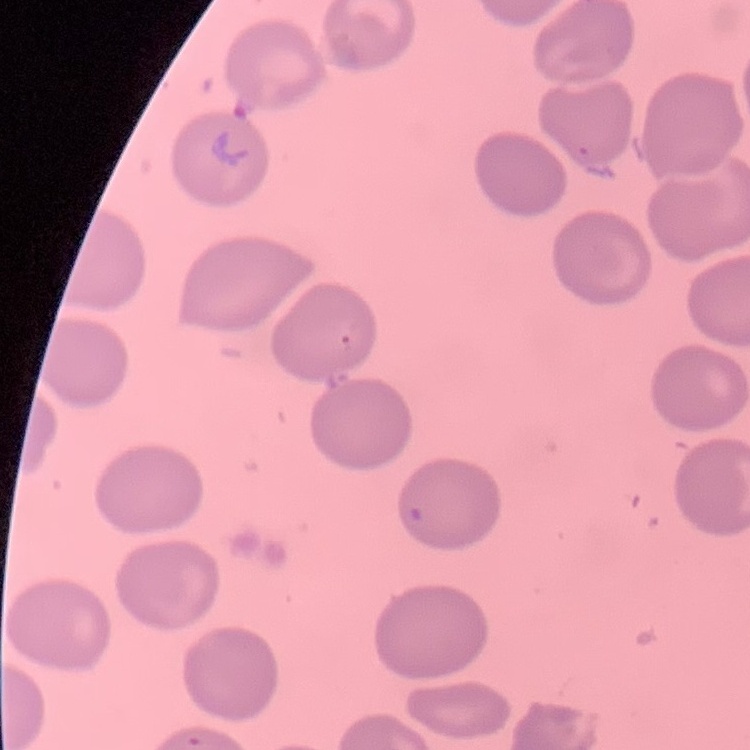
Summary:
  - Erythrocyte morphology: no rouleaux formation
  - Preparation: thin blood smear
  - Image type: one tile cut from a larger photomicrograph
  - Stain: Field's or Giemsa